Identify the parasite.
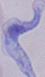
This is a trypanosome.

modality = micrograph
magnification = 1000x